Report the malaria status of this cell.
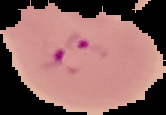
It is parasitized.

image type = cell region segmented out of the field of view; surrounding area masked to black
image size = 166×115 pixels
preparation = thin blood film